Assess this cell for malaria.
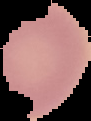
It is uninfected.

image type = cell region segmented out of the field of view; surrounding area masked to black
image size = 91×121 pixels
preparation = thin blood film